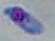
Summary:
  - Identification: Toxoplasma gondii
  - Magnification: 1000x
  - Modality: photomicrograph